Outline each blood parasite and name the species.
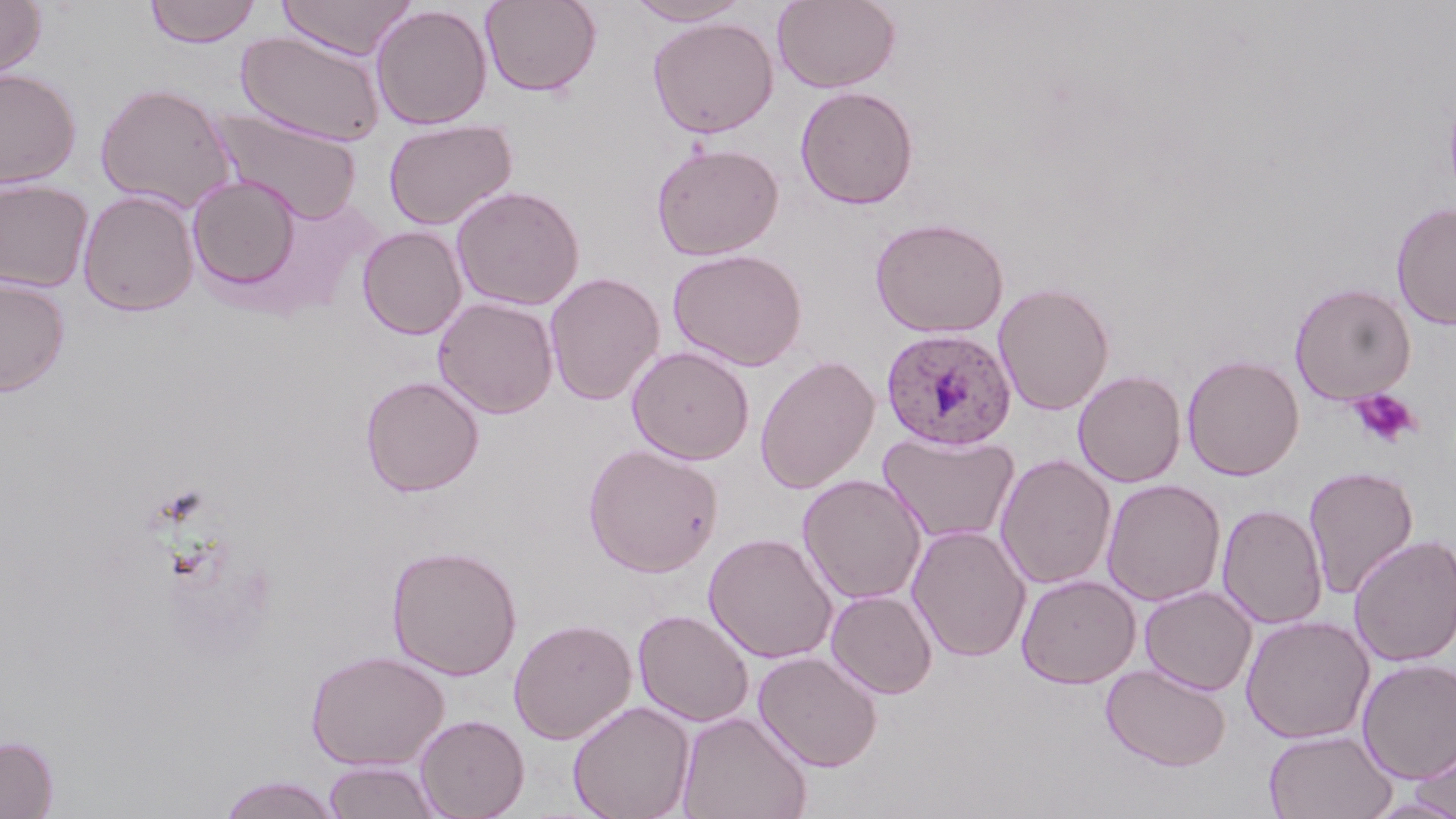

Approximate bounding boxes as [x1, y1, x2, y2] in pixels.
Plasmodium ovale-infected red blood cells: [880, 327, 1017, 451].
No Plasmodium falciparum, Plasmodium malariae, Plasmodium vivax, Babesia divergens, or Trypanosoma brucei observed.

{
  "slide_level_diagnosis": "Plasmodium ovale",
  "modality": "optical microscopy",
  "preparation": "thin blood film",
  "image_size": "1456×819 pixels",
  "stain": "May-Grünwald-Giemsa",
  "platelet_locations": "approximate bounding boxes as [x1, y1, x2, y2] in pixels: [1349, 388, 1421, 449]",
  "field_of_view": "one of a larger specimen",
  "magnification": "1000x",
  "uninfected_red_blood_cell_locations": "approximate bounding boxes as [x1, y1, x2, y2] in pixels: [0, 0, 47, 83], [143, 0, 263, 47], [274, 0, 418, 60], [480, 0, 601, 97], [624, 0, 753, 26], [771, 0, 900, 94], [370, 4, 492, 130], [647, 16, 779, 138], [237, 30, 386, 146], [0, 67, 82, 189], [94, 81, 239, 214], [795, 85, 919, 210], [212, 108, 363, 225], [383, 118, 518, 231], [651, 141, 784, 261], [186, 175, 303, 296], [0, 178, 94, 293], [451, 185, 585, 310], [77, 189, 200, 317], [1391, 202, 1456, 329], [870, 217, 1010, 338], [357, 226, 468, 340], [668, 249, 808, 370], [544, 272, 665, 405], [0, 275, 70, 397], [993, 282, 1114, 416], [1289, 283, 1416, 404], [433, 297, 559, 419], [627, 345, 755, 465], [1182, 353, 1304, 481], [755, 355, 879, 493], [1073, 370, 1186, 487], [360, 375, 485, 497], [877, 430, 1020, 545], [583, 441, 724, 578], [995, 453, 1117, 590], [1303, 465, 1419, 599], [797, 473, 927, 605], [1102, 478, 1226, 606], [1216, 503, 1328, 629], [907, 524, 1032, 662], [703, 532, 838, 664], [1349, 534, 1456, 667], [386, 545, 523, 681], [1016, 574, 1141, 688], [1139, 585, 1257, 695], [826, 589, 938, 698], [632, 608, 755, 727], [1241, 615, 1375, 744], [508, 617, 637, 745], [305, 649, 448, 770], [753, 651, 883, 772], [1357, 659, 1456, 784], [1101, 663, 1231, 772], [567, 700, 696, 819], [676, 710, 813, 819], [415, 714, 530, 819], [1410, 728, 1456, 816], [1264, 729, 1397, 819], [0, 735, 59, 819], [322, 760, 444, 819], [215, 775, 345, 818], [1364, 796, 1456, 818]"
}